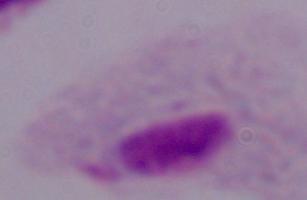
Captured at 1000x magnification. Micrograph. A trichomonad is shown.